Classify this cell by malaria status.
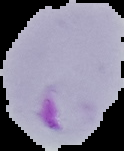

It is parasitized.

image_type: segmented cell region on a black background
image_size: 124×151 pixels
preparation: thin blood smear